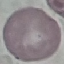
{
  "malaria_status": "uninfected",
  "capture": "smartphone camera at the microscope eyepiece",
  "image_type": "automatically extracted cell patch, resized to 64 × 64 pixels",
  "stain": "Giemsa",
  "preparation": "thin blood film"
}